Outline each uninfected red blood cell.
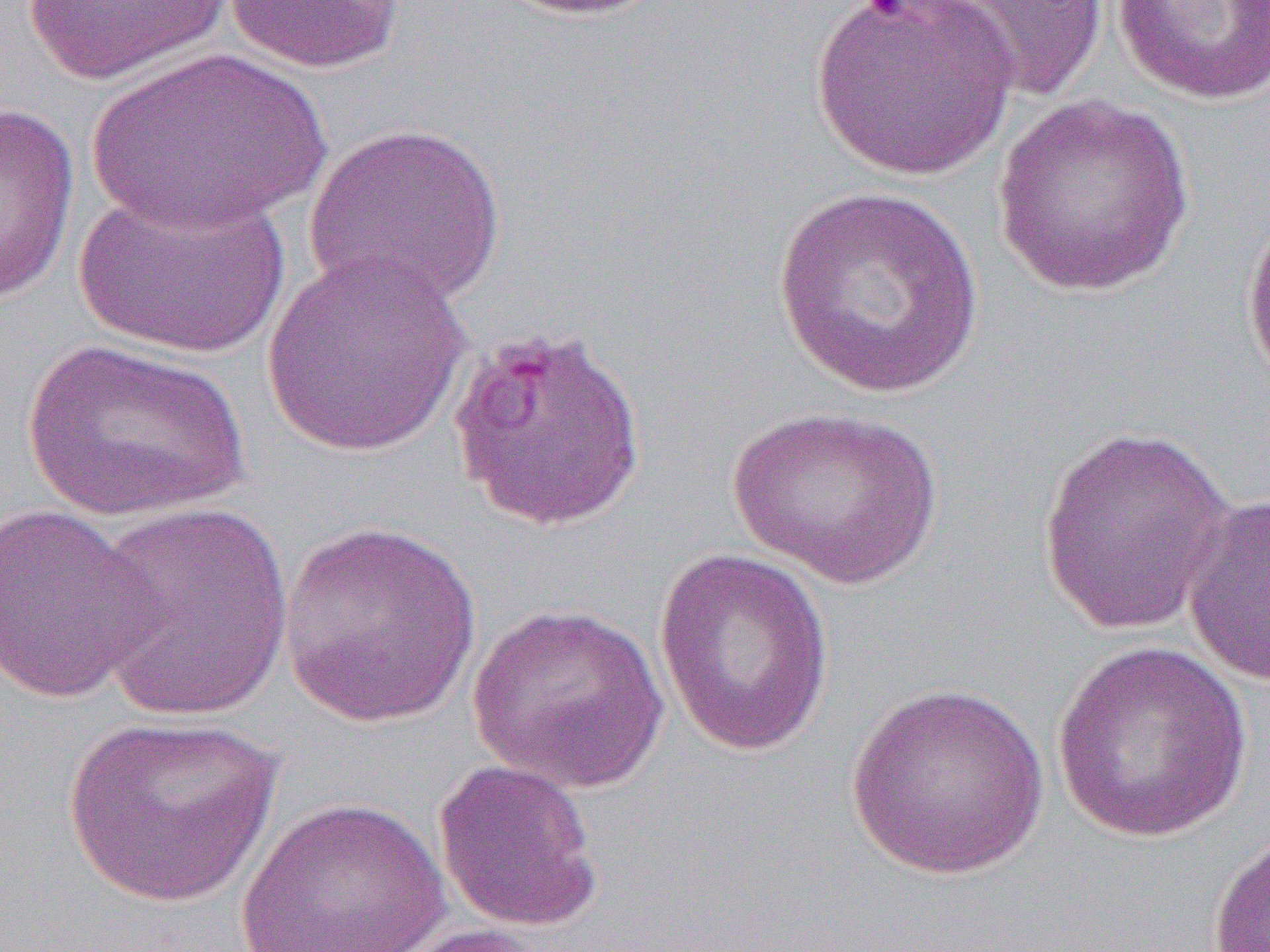
Approximate bounding boxes as (x1, y1, x2, y2) in pixels.
Uninfected red blood cells (subset): (20, 0, 235, 85), (490, 0, 673, 21), (808, 0, 1016, 181), (923, 0, 1111, 103), (1111, 0, 1270, 106), (222, 1, 405, 75), (86, 44, 330, 232), (991, 96, 1196, 298), (0, 101, 80, 307), (302, 121, 508, 310), (72, 183, 292, 360), (770, 183, 987, 400), (1239, 205, 1270, 396), (260, 250, 473, 460), (24, 338, 252, 524), (727, 404, 946, 591), (1036, 426, 1237, 638), (1181, 493, 1270, 688), (0, 501, 163, 704), (88, 503, 298, 723), (276, 521, 482, 729), (654, 548, 835, 756), (466, 602, 670, 795), (1050, 640, 1253, 844), (844, 682, 1051, 882), (61, 713, 282, 909), (433, 759, 604, 933), (235, 796, 451, 951), (1208, 830, 1270, 951), (371, 922, 554, 952).

{
  "slide_level_diagnosis": "Plasmodium falciparum",
  "image_size": "1270×952 pixels",
  "magnification": "1000x",
  "modality": "light microscopy",
  "field_of_view": "single",
  "preparation": "thin blood film"
}